Classify this cell by malaria status.
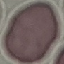

Uninfected.

{
  "capture": "smartphone camera at the microscope eyepiece",
  "image_type": "cell patch, automatically extracted from a larger field of view and resized to 64 × 64 pixels",
  "preparation": "thin blood smear",
  "stain": "Giemsa"
}